Assess this cell for malaria.
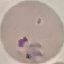
It is parasitized.

{
  "preparation": "thin blood film",
  "stain": "Giemsa",
  "image_type": "cell patch, automatically extracted from a larger field of view and resized to 64 × 64 pixels",
  "capture": "smartphone through the microscope eyepiece"
}